Outline each Plasmodium vivax-infected red blood cell.
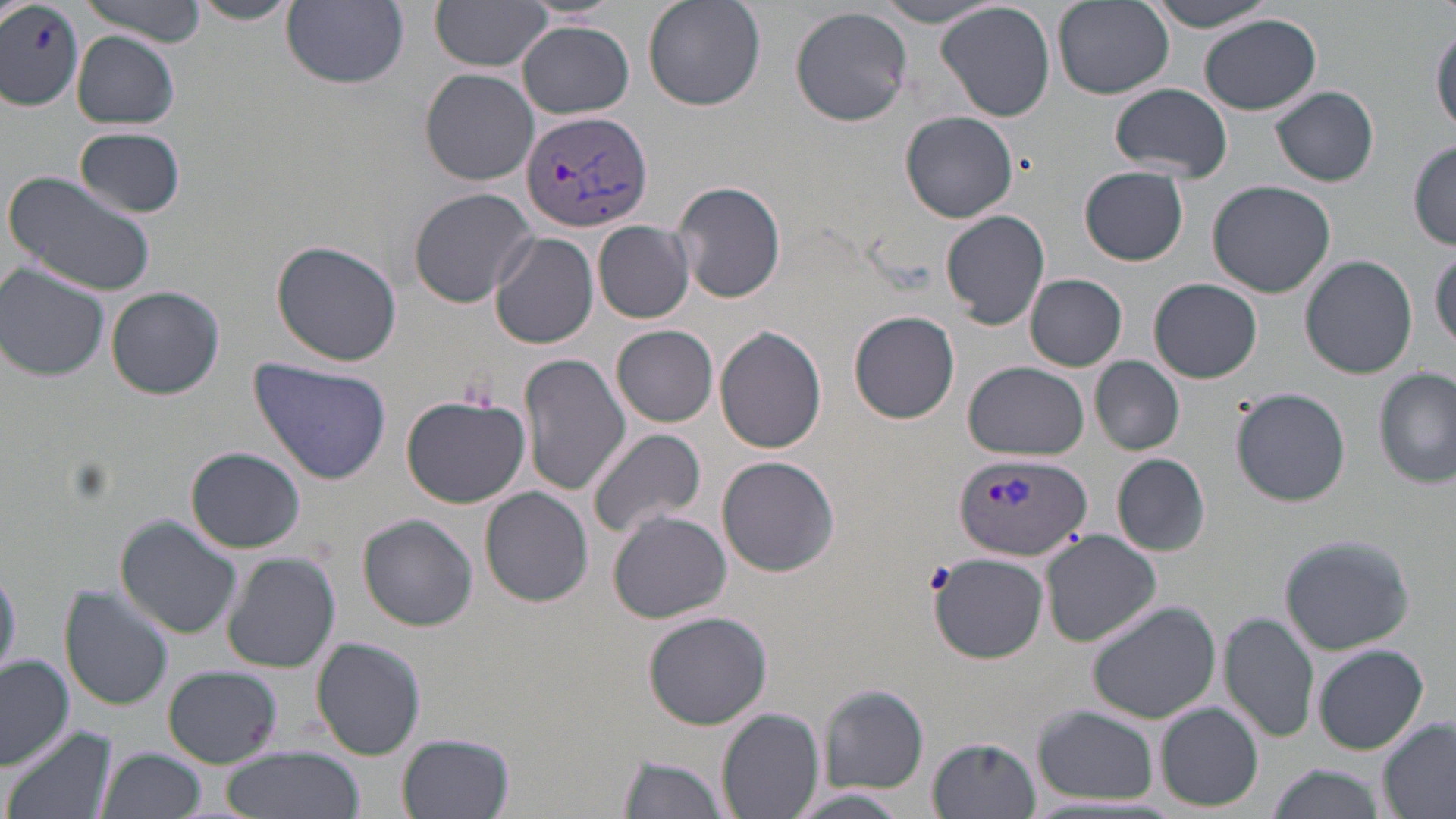

Approximate bounding boxes as (x1, y1, x2, y2) in pixels.
Plasmodium vivax-infected red blood cells: (519, 108, 653, 233), (955, 451, 1091, 563).

Uninfected red blood cell locations: (78, 0, 207, 42), (1144, 0, 1285, 32), (282, 1, 409, 88), (430, 1, 555, 72), (641, 1, 764, 110), (872, 1, 1007, 27), (1052, 1, 1174, 100), (185, 2, 300, 25), (936, 2, 1055, 123), (0, 5, 85, 108), (790, 7, 914, 126), (1199, 15, 1321, 116), (518, 20, 633, 118), (1430, 22, 1456, 135), (72, 33, 181, 128), (420, 68, 541, 186), (1110, 84, 1234, 180), (1271, 86, 1379, 186), (901, 112, 1019, 223), (76, 127, 186, 217), (1408, 142, 1455, 250), (1080, 168, 1189, 265), (1, 170, 158, 296), (672, 179, 788, 304), (1208, 180, 1334, 298), (408, 187, 537, 306), (941, 210, 1050, 329), (593, 220, 696, 323), (488, 232, 599, 349), (272, 241, 404, 367), (1430, 246, 1456, 349), (1301, 254, 1418, 378), (0, 265, 109, 381), (1025, 274, 1127, 371), (1148, 278, 1262, 383), (107, 286, 224, 400), (849, 311, 960, 424), (612, 325, 718, 427), (714, 325, 828, 453), (518, 352, 628, 496), (1090, 356, 1185, 455), (248, 357, 393, 485), (963, 363, 1093, 460), (1374, 368, 1454, 489), (1233, 388, 1350, 506), (401, 393, 529, 509), (587, 426, 708, 539), (186, 446, 305, 553), (1113, 454, 1208, 557), (716, 456, 839, 576), (480, 485, 594, 607), (606, 510, 731, 622), (358, 514, 478, 631), (115, 516, 242, 640), (1039, 530, 1162, 647), (1274, 531, 1419, 655), (225, 552, 340, 675), (931, 553, 1049, 663), (0, 559, 20, 680), (59, 587, 175, 710), (1086, 599, 1224, 723), (641, 609, 771, 729), (1221, 612, 1318, 742), (311, 636, 426, 758), (1315, 644, 1429, 756), (0, 655, 74, 770), (162, 666, 282, 768), (819, 684, 928, 791), (1157, 702, 1263, 811), (1031, 706, 1158, 805), (718, 707, 823, 818), (1377, 717, 1455, 818), (5, 725, 116, 819), (398, 732, 514, 818), (929, 736, 1041, 817), (95, 746, 206, 819), (219, 746, 364, 819), (615, 754, 732, 819), (1266, 764, 1387, 819), (785, 787, 916, 818). Slide-level diagnosis: Plasmodium vivax. Light microscopy. May-Grünwald-Giemsa stain. Image is 1456×819 pixels. One field of a larger specimen. 1000x magnification. Thin blood film.